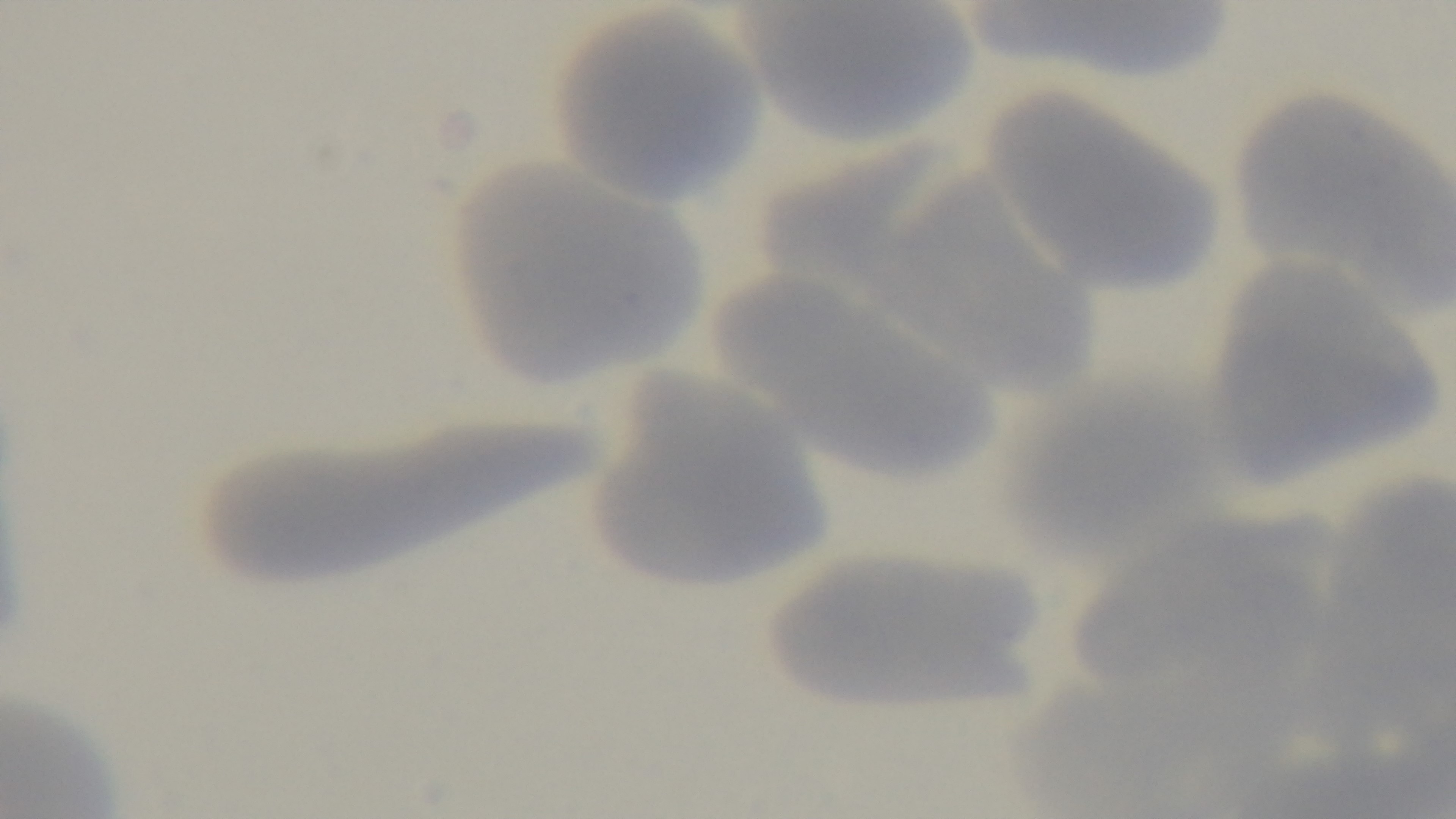

{
  "objective": "100x oil immersion",
  "capture": "mounted 4K digital camera",
  "preparation": "thin blood film",
  "malaria_status": "uninfected",
  "modality": "light microscopy",
  "field_of_view": "one from the slide",
  "stain": "Giemsa"
}